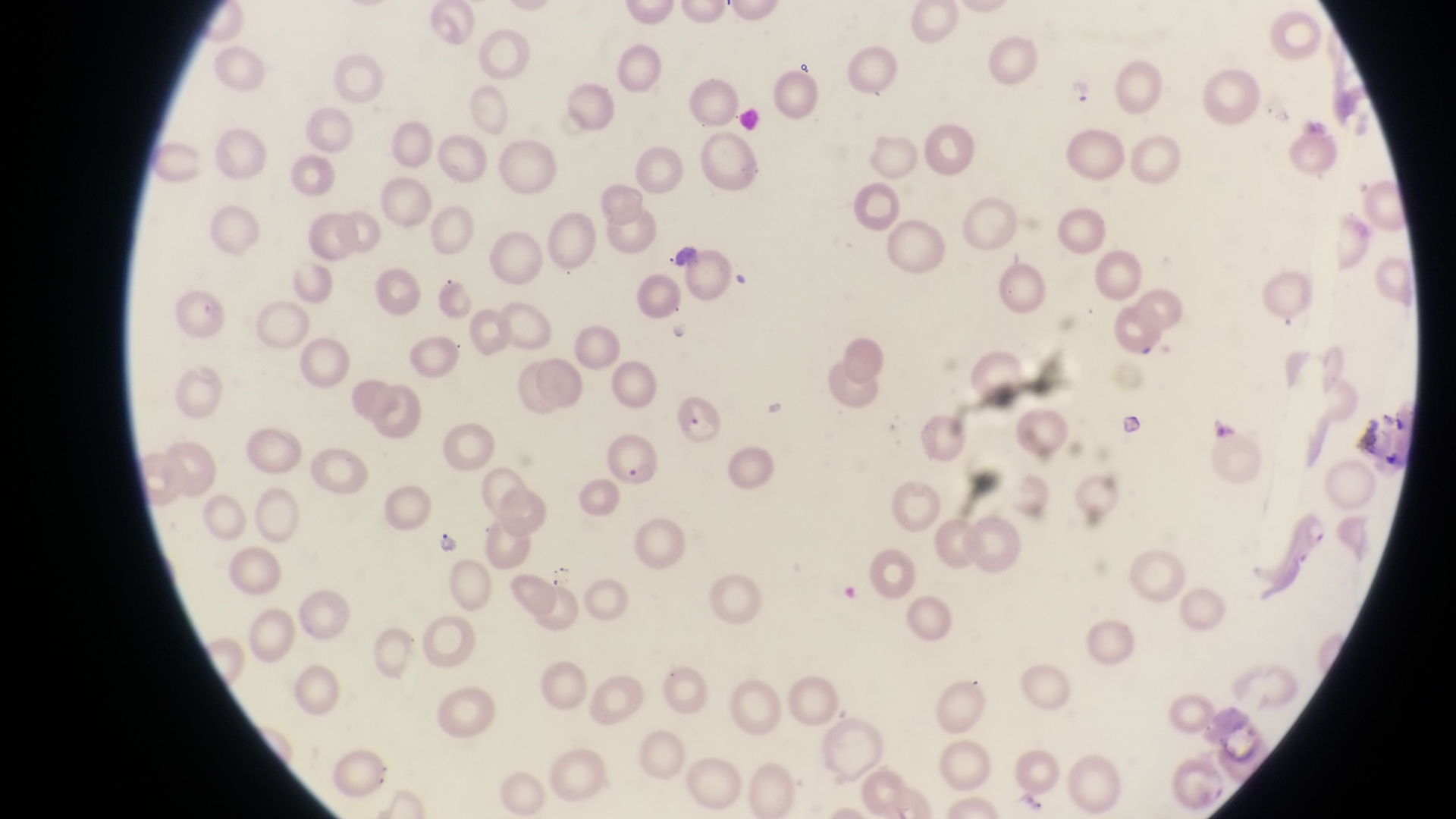 Approximate bounding boxes as [left, top, right, bottom] in pixels. Parasitised red blood cell locations: [605, 429, 661, 484], [1288, 507, 1331, 559]. Trophozoite locations: [1065, 74, 1098, 107], [430, 528, 466, 558]. Artifact (platelet-like body, stain precipitate, or debris) locations: [793, 58, 823, 81], [1116, 412, 1146, 442]. Captured by a smartphone held over the eyepiece of an Olympus CX-23 microscope. Sample from Uganda. Thin blood film. Single field of view. Image is 1456×819 pixels. At a magnification of 1000x.